Point out each malaria parasite.
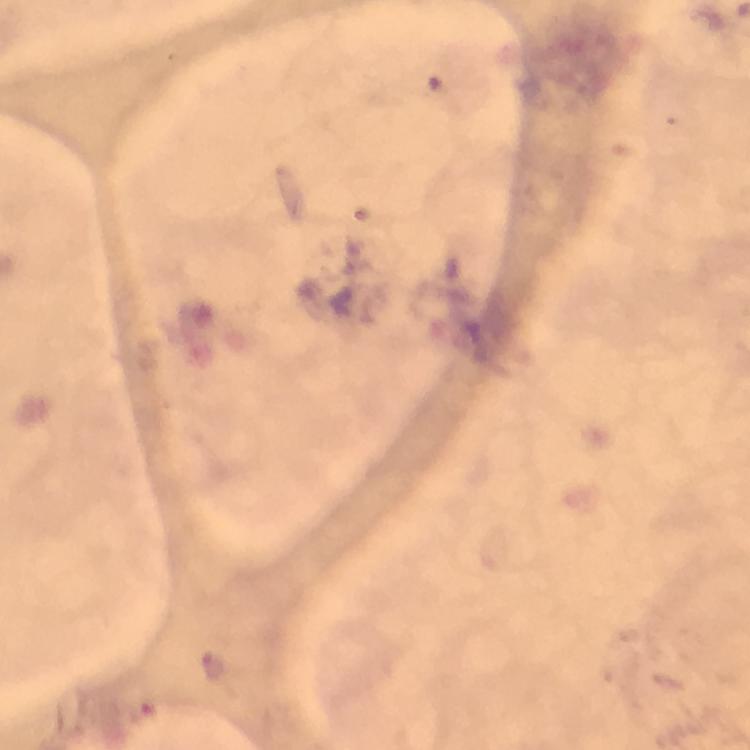

Approximate object centers, in pixels from the top-left corner.
Malaria parasites: (x=211, y=667).

image size = 750×750 pixels
preparation = thick blood film
capture = smartphone mounted on the microscope
cropped from = one field of view
immersion oil = applied
context = from a malaria diagnostic workup
stain = Giemsa
magnification = 100x